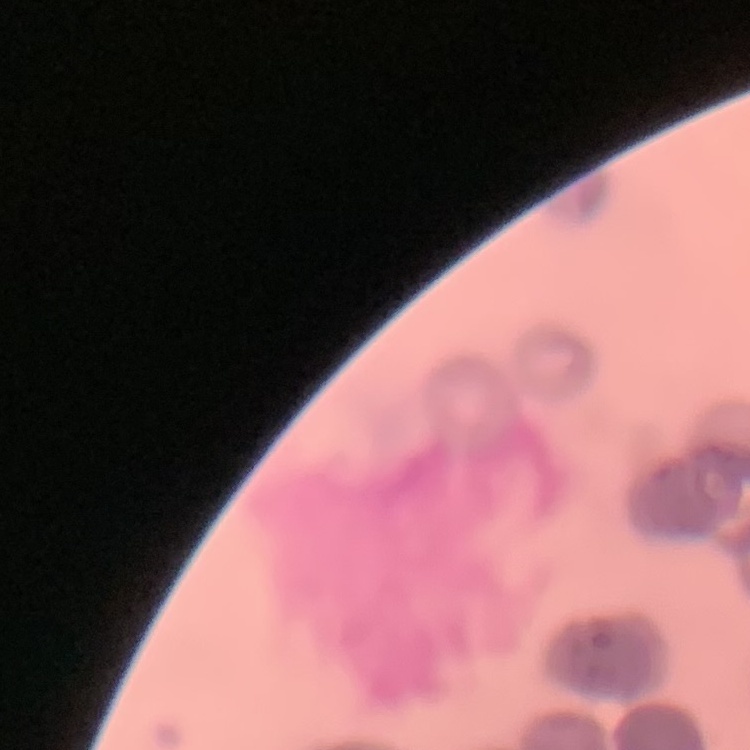

Summary:
  - Erythrocyte morphology: rouleaux formation
  - Stain: Field's or Giemsa
  - Image type: square crop of a larger photomicrograph
  - Preparation: thin blood smear